Describe the morphology of the erythrocytes.
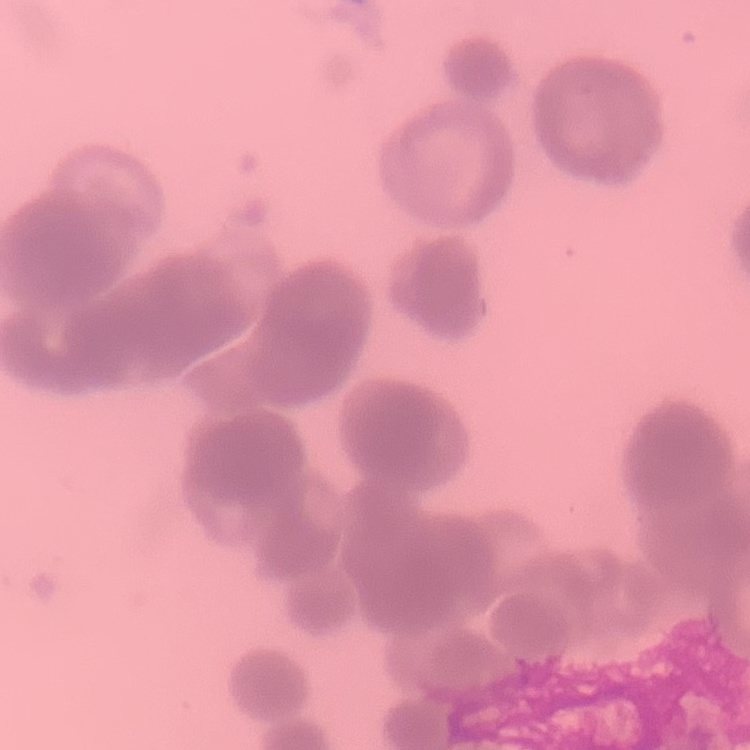

They show rouleaux formation.

image type = square crop of a larger photomicrograph
stain = Field's or Giemsa
preparation = thin blood film